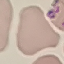
Malaria status: uninfected. Automatically extracted cell patch, resized to 64 × 64 pixels. Giemsa-stained preparation. Thin smear of blood. Acquired by smartphone through the microscope eyepiece.